Give the position of every Plasmodium parasite.
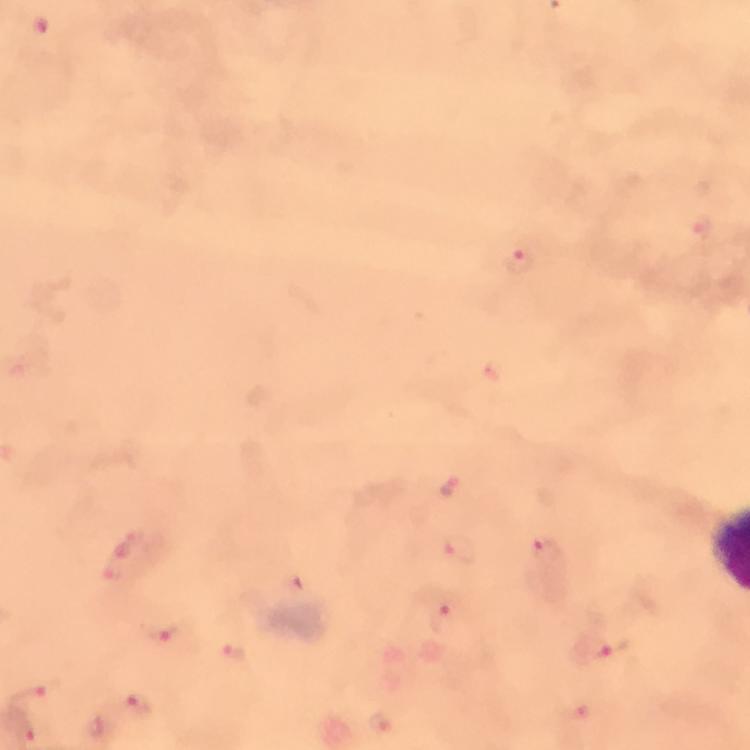

Approximate centers as {x, y} in pixels.
Plasmodium parasites: {698, 227}, {519, 261}, {448, 487}, {545, 550}, {460, 551}, {135, 555}, {443, 620}, {164, 632}, {597, 649}, {234, 655}, {31, 696}, {137, 705}, {575, 712}.

preparation = thick smear
immersion oil = used
image size = 750×750 pixels
capture = smartphone mounted on the microscope
magnification = 100x
stain = Giemsa
context = from a malaria diagnostic workup
cropped from = one field of view